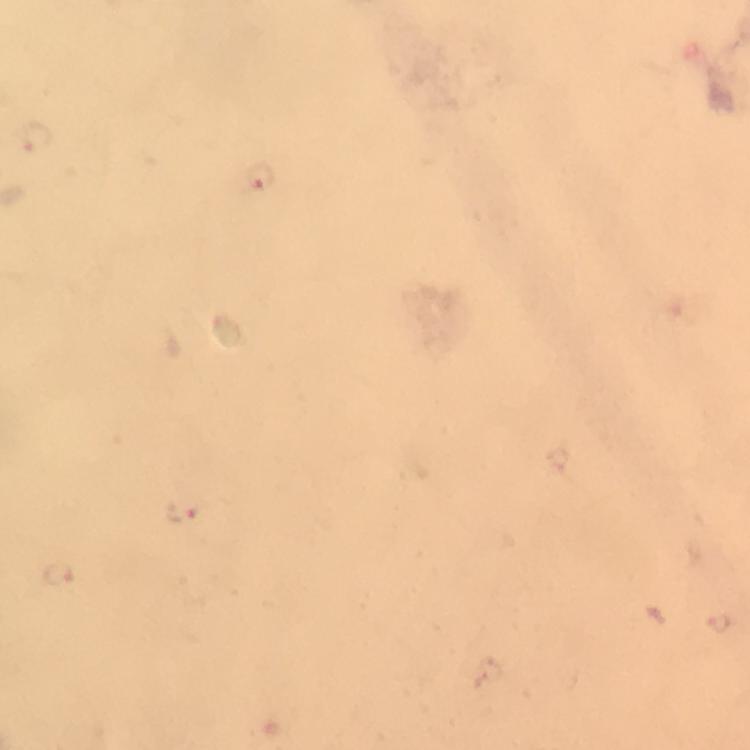
Approximate centers as [x, y] in pixels. Malaria parasite locations: [260, 175], [183, 511], [59, 573], [721, 623]. Thick blood film. At 100x magnification. A crop from one field of view. Smartphone photograph taken through a microscope. Giemsa stain. From a diagnostic examination for malaria. Immersion oil applied. Image is 750×750 pixels.